Classify this cell by malaria status.
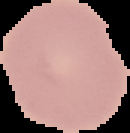

Uninfected.

From a thin blood film. Image is 130×133 pixels. The area outside the segmented cell region is set to black.